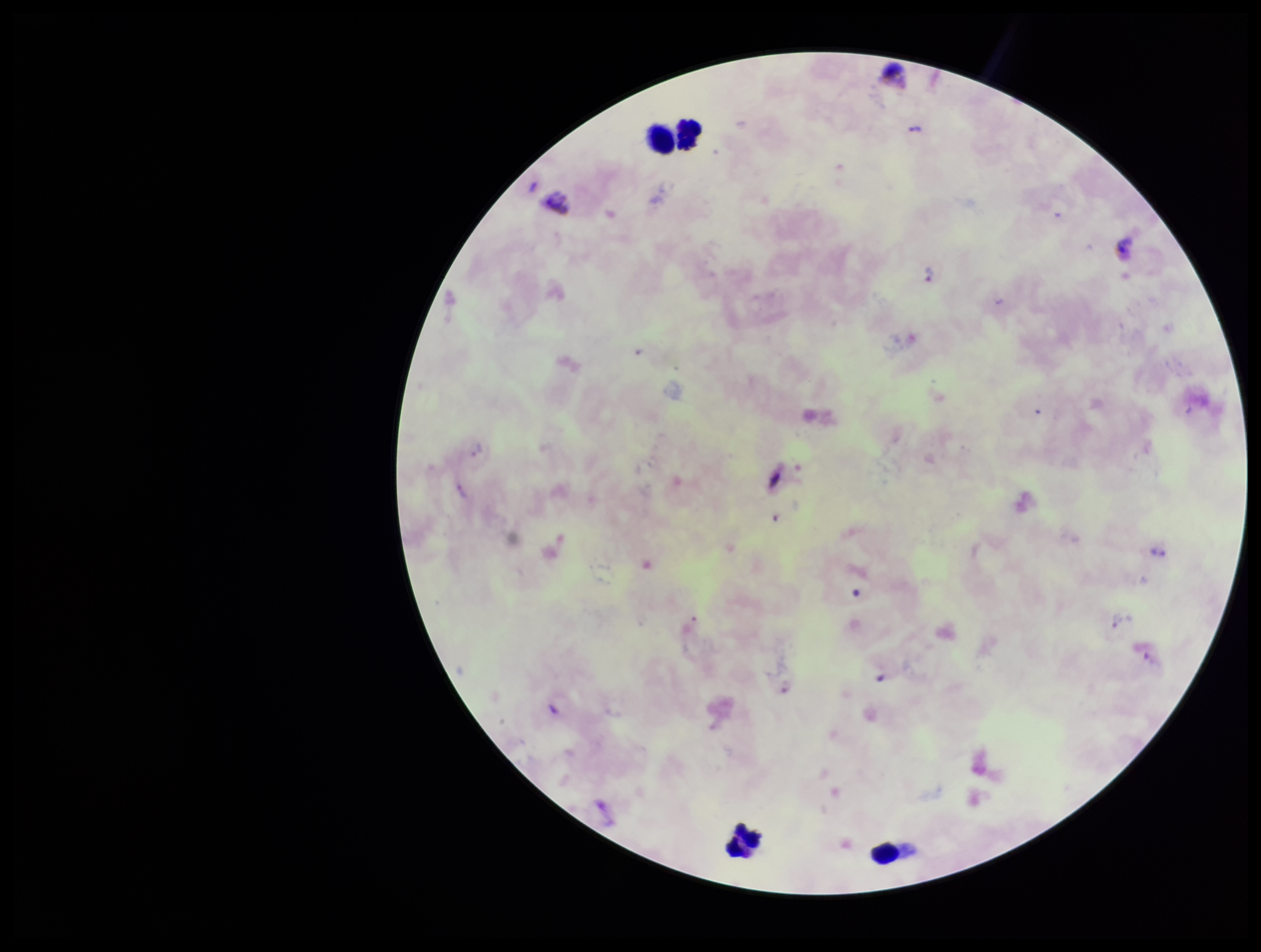
One field from this slide. Leukocyte count: 4. Image is 1261×952 pixels. Species reported for this patient: Plasmodium vivax. Smartphone photograph taken through the eyepiece of a microscope. Preparation: thick blood smear. Patient malaria status: positive. Plasmodium parasites: detected. Stained with Giemsa. Parasite count: 3.